Classify this cell by malaria status.
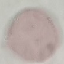

Uninfected.

Summary:
  - Stain: Giemsa
  - Capture: smartphone camera at the microscope eyepiece
  - Preparation: thin blood film
  - Image type: cell patch, automatically extracted from a larger field of view and resized to 64 × 64 pixels